Assess the morphology of the erythrocytes.
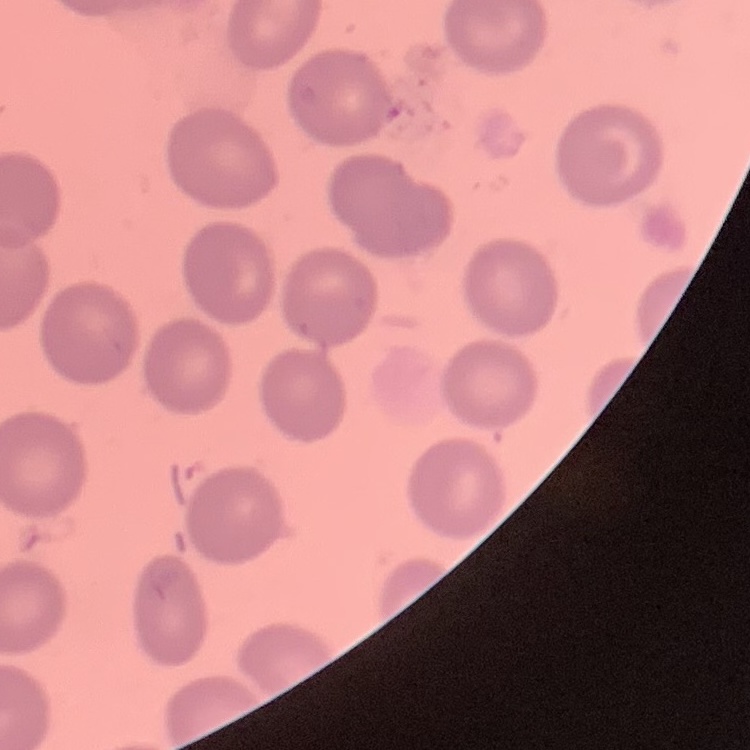

They show no rouleaux formation.

Thin peripheral smear. One tile cut from a larger photomicrograph. Stained with either Field's or Giemsa.